Assess for Plasmodium parasites.
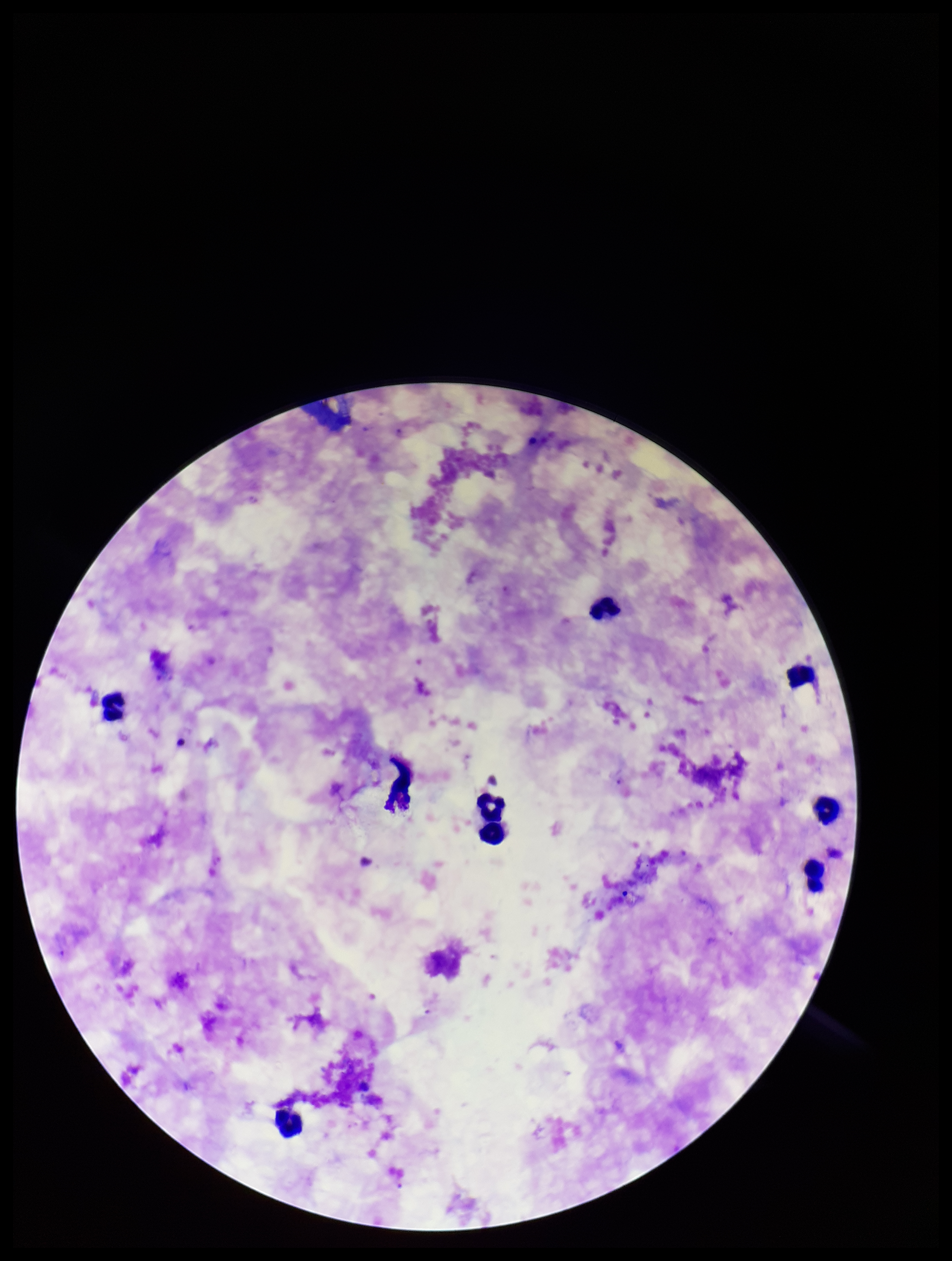

Seen.

patient_malaria_status: positive
preparation: thick smear
stain: Giemsa
parasite_count: 1
image_size: 952×1261 pixels
field_of_view: single
capture: smartphone photograph through the microscope eyepiece
species_reported_for_this_patient: Plasmodium falciparum
leukocyte_count: 9